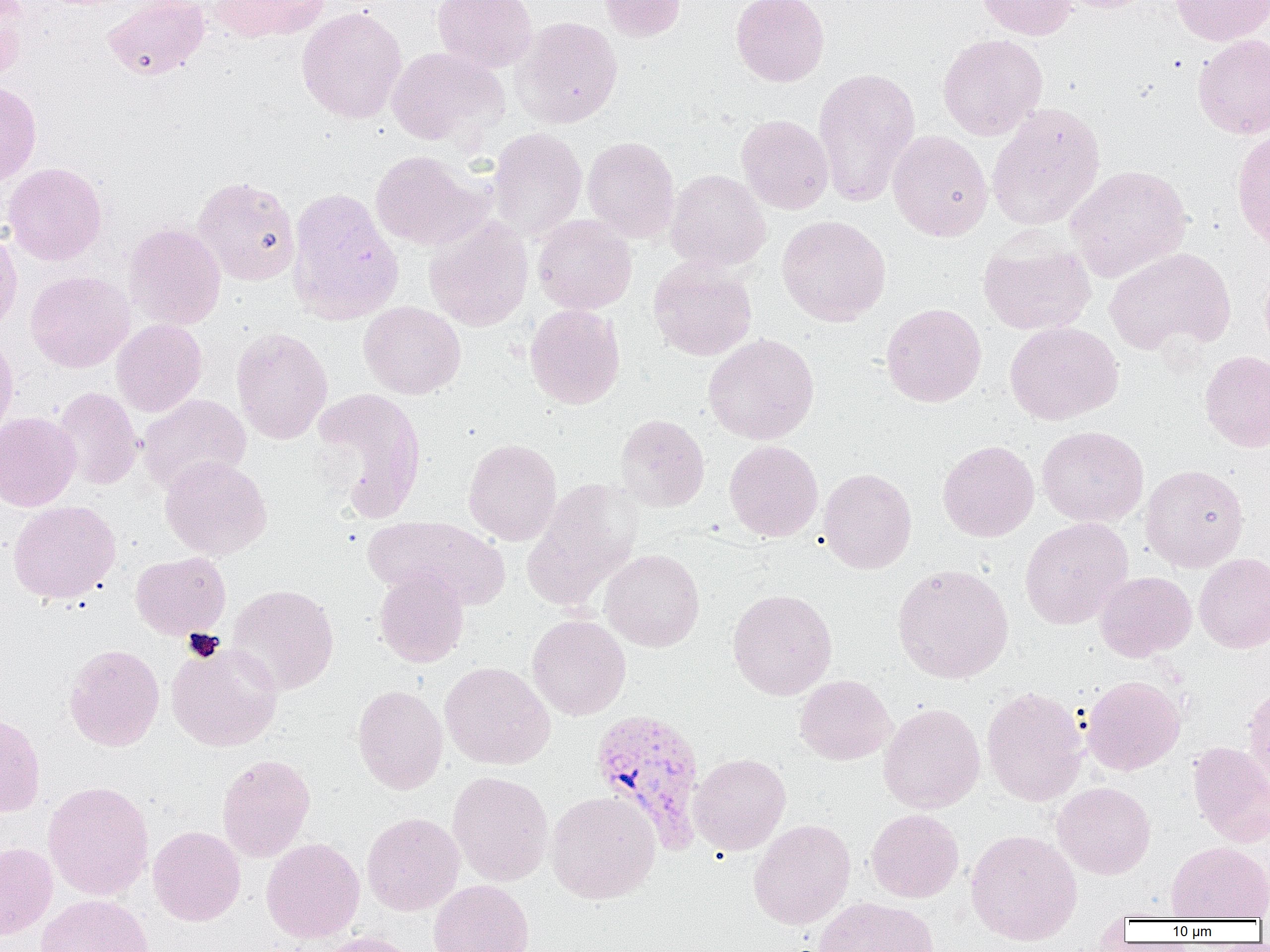
{
  "slide_level_diagnosis": "Plasmodium vivax",
  "uninfected_red_blood_cell_locations": "approximate bounding boxes as (x1,y1)-(x2,y2) corner pairs in pixels: (0,0)-(30,81), (101,0)-(210,80), (211,0)-(329,42), (432,0)-(538,73), (598,0)-(686,42), (731,0)-(829,87), (975,0)-(1077,40), (1053,0)-(1157,13), (1169,0)-(1270,46), (296,6)-(407,124), (512,16)-(623,128), (1193,33)-(1270,139), (937,34)-(1048,141), (386,46)-(507,146), (812,67)-(921,208), (0,82)-(41,187), (986,102)-(1106,231), (736,114)-(834,214), (1232,125)-(1270,252), (487,127)-(587,241), (888,130)-(993,241), (582,136)-(680,242), (369,150)-(490,250), (3,162)-(107,265), (1066,164)-(1192,282), (665,169)-(771,273), (192,175)-(301,286), (286,187)-(403,325), (424,215)-(534,331), (776,215)-(891,326), (532,216)-(637,315), (124,222)-(226,330), (0,225)-(22,337), (977,234)-(1095,335), (1104,247)-(1236,356), (648,258)-(757,361), (25,270)-(134,372), (358,301)-(466,399), (881,302)-(986,407), (525,304)-(625,409), (111,319)-(207,416), (1005,321)-(1123,425), (231,326)-(333,444), (0,331)-(18,442), (703,333)-(820,445), (1200,350)-(1270,452), (311,386)-(428,524), (54,387)-(142,490), (138,393)-(251,493), (0,411)-(80,511), (615,413)-(709,512), (1037,426)-(1149,527), (463,438)-(562,545), (724,440)-(823,542), (938,440)-(1039,542), (160,456)-(272,560), (1140,464)-(1249,573), (818,468)-(917,574), (523,479)-(641,611), (8,500)-(121,604), (362,515)-(510,610), (1020,517)-(1133,629), (600,548)-(705,652), (130,551)-(231,640), (1194,552)-(1270,653), (892,563)-(1014,683), (374,567)-(469,668), (1095,571)-(1196,661), (227,583)-(340,695), (727,588)-(837,700), (527,614)-(631,720), (166,641)-(283,751), (64,643)-(164,751), (440,661)-(555,769), (794,674)-(896,764), (1081,675)-(1186,775), (1242,682)-(1270,794), (352,684)-(448,794), (981,686)-(1088,807), (878,702)-(986,813), (0,712)-(45,817), (1188,742)-(1270,847), (689,752)-(791,855), (217,754)-(315,861), (448,770)-(553,886), (43,780)-(154,900), (1052,782)-(1156,879), (547,790)-(661,904), (866,809)-(964,902), (361,812)-(464,916), (748,819)-(856,929), (148,825)-(246,926), (965,828)-(1082,944), (261,838)-(365,942), (1166,841)-(1270,920), (0,842)-(57,939), (428,879)-(535,952), (35,893)-(153,952), (813,896)-(938,952), (313,931)-(422,952)",
  "field_of_view": "single",
  "magnification": "1000x",
  "preparation": "thin blood smear",
  "plasmodium_vivax_infected_red_blood_cell_locations": "approximate bounding boxes as (x1,y1)-(x2,y2) corner pairs in pixels: (590,709)-(706,853)",
  "image_size": "1270×952 pixels",
  "modality": "optical microscopy"
}